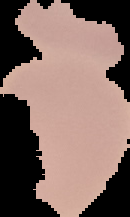

Summary:
  - Preparation: thin blood smear
  - Image type: cell region segmented out of the field of view; surrounding area masked to black
  - Malaria status: uninfected
  - Image size: 130×217 pixels